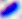
Summary:
  - Identification: Toxoplasma gondii
  - Magnification: 400x
  - Modality: micrograph